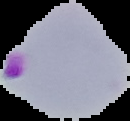
Summary:
  - Image size: 130×121 pixels
  - Image type: cell region segmented out of the field of view; surrounding area masked to black
  - Preparation: thin blood smear
  - Result: Plasmodium parasites identified